Assess this cell for malaria.
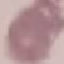
Uninfected.

capture: smartphone camera at the microscope eyepiece
stain: Giemsa
image_type: cell patch, automatically extracted from a larger field of view and resized to 64 × 64 pixels
preparation: thin blood smear